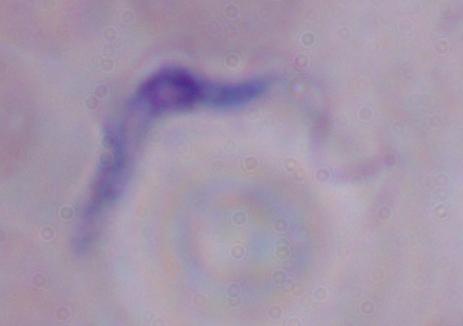

Micrograph. A trypanosome is shown. 1000x magnification.